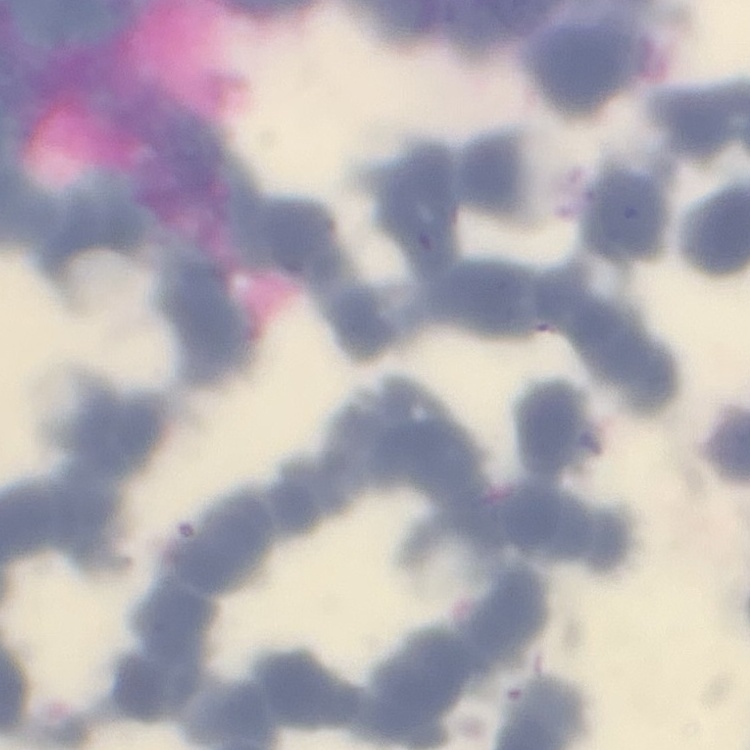

The erythrocytes exhibit rouleaux formation. One tile cut from a larger photomicrograph. Stained with either Field's or Giemsa. Thin blood smear.